Identify the parasite.
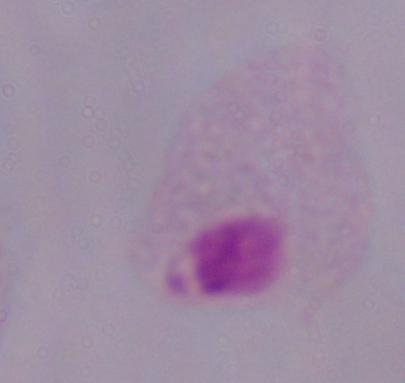
A trichomonad.

Summary:
  - Modality: micrograph
  - Magnification: 1000x